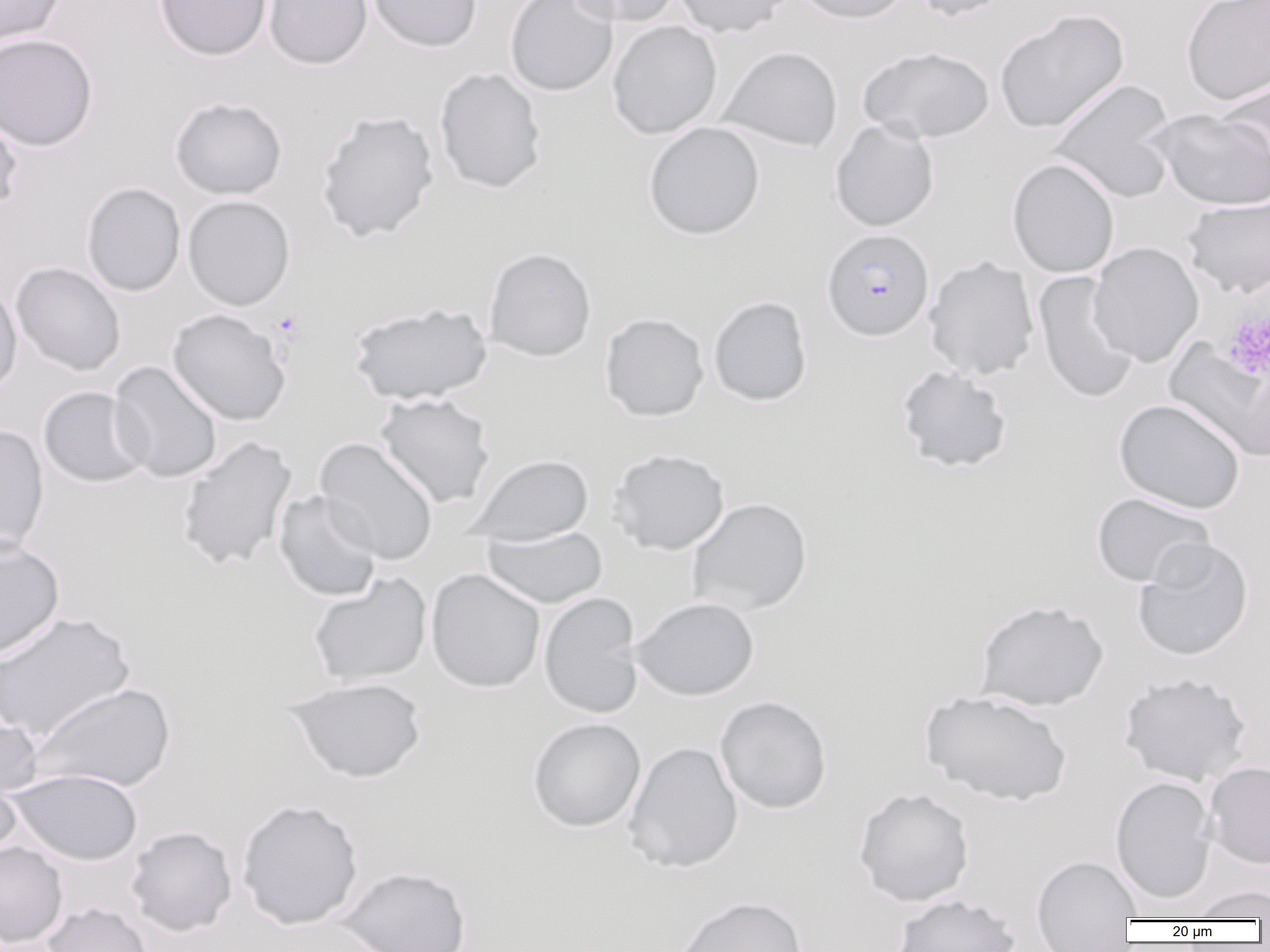
Summary:
  - Coordinate format: approximate bounding boxes as named x1/y1/x2/y2 corners in pixels
  - Platelet locations: (x1=1222, y1=309, x2=1270, y2=379)
  - Plasmodium falciparum-infected red blood cell locations: (x1=822, y1=228, x2=934, y2=341)
  - Uninfected red blood cell locations: (x1=0, y1=0, x2=67, y2=48), (x1=153, y1=0, x2=273, y2=61), (x1=263, y1=0, x2=372, y2=70), (x1=367, y1=0, x2=482, y2=53), (x1=504, y1=0, x2=620, y2=97), (x1=567, y1=0, x2=682, y2=27), (x1=673, y1=0, x2=793, y2=37), (x1=795, y1=0, x2=914, y2=24), (x1=909, y1=0, x2=1017, y2=22), (x1=1181, y1=0, x2=1270, y2=105), (x1=994, y1=8, x2=1130, y2=134), (x1=607, y1=21, x2=723, y2=139), (x1=0, y1=33, x2=99, y2=151), (x1=858, y1=45, x2=995, y2=144), (x1=719, y1=46, x2=843, y2=153), (x1=434, y1=67, x2=547, y2=194), (x1=1215, y1=77, x2=1270, y2=185), (x1=1049, y1=79, x2=1179, y2=203), (x1=169, y1=96, x2=288, y2=200), (x1=0, y1=107, x2=24, y2=217), (x1=1147, y1=108, x2=1270, y2=210), (x1=315, y1=110, x2=440, y2=242), (x1=829, y1=119, x2=940, y2=232), (x1=643, y1=122, x2=765, y2=240), (x1=1007, y1=158, x2=1120, y2=278), (x1=81, y1=182, x2=186, y2=297), (x1=182, y1=195, x2=295, y2=311), (x1=1182, y1=195, x2=1269, y2=299), (x1=1088, y1=242, x2=1204, y2=367), (x1=484, y1=247, x2=597, y2=361), (x1=923, y1=256, x2=1040, y2=382), (x1=10, y1=262, x2=126, y2=376), (x1=1033, y1=271, x2=1140, y2=404), (x1=0, y1=281, x2=22, y2=398), (x1=708, y1=295, x2=813, y2=407), (x1=348, y1=302, x2=492, y2=405), (x1=166, y1=309, x2=291, y2=426), (x1=600, y1=313, x2=709, y2=422), (x1=1166, y1=340, x2=1270, y2=461), (x1=109, y1=361, x2=223, y2=483), (x1=894, y1=364, x2=1014, y2=474), (x1=38, y1=386, x2=150, y2=488), (x1=375, y1=392, x2=496, y2=508), (x1=1113, y1=399, x2=1247, y2=514), (x1=0, y1=425, x2=49, y2=557), (x1=175, y1=436, x2=297, y2=572), (x1=315, y1=437, x2=439, y2=566), (x1=607, y1=448, x2=730, y2=555), (x1=467, y1=454, x2=594, y2=545), (x1=273, y1=490, x2=382, y2=602), (x1=1091, y1=492, x2=1215, y2=589), (x1=687, y1=497, x2=813, y2=616), (x1=481, y1=525, x2=608, y2=609), (x1=0, y1=536, x2=65, y2=661), (x1=1132, y1=538, x2=1255, y2=662), (x1=426, y1=569, x2=546, y2=693), (x1=307, y1=573, x2=432, y2=688), (x1=538, y1=591, x2=645, y2=719), (x1=632, y1=596, x2=759, y2=701), (x1=974, y1=599, x2=1109, y2=711), (x1=0, y1=611, x2=136, y2=744), (x1=1118, y1=671, x2=1254, y2=786), (x1=285, y1=677, x2=427, y2=783), (x1=29, y1=682, x2=176, y2=794), (x1=920, y1=690, x2=1073, y2=806), (x1=714, y1=696, x2=833, y2=814), (x1=0, y1=709, x2=44, y2=801), (x1=526, y1=717, x2=646, y2=833), (x1=622, y1=741, x2=743, y2=873), (x1=0, y1=760, x2=23, y2=863), (x1=1204, y1=761, x2=1270, y2=870), (x1=6, y1=768, x2=143, y2=866), (x1=1109, y1=776, x2=1218, y2=905), (x1=853, y1=786, x2=975, y2=907), (x1=237, y1=799, x2=363, y2=930), (x1=125, y1=825, x2=237, y2=936), (x1=0, y1=841, x2=68, y2=949), (x1=1031, y1=854, x2=1143, y2=950), (x1=335, y1=865, x2=472, y2=952), (x1=1187, y1=885, x2=1269, y2=920), (x1=891, y1=893, x2=1021, y2=952), (x1=671, y1=895, x2=808, y2=952), (x1=41, y1=902, x2=154, y2=952)
  - Slide-level diagnosis: Plasmodium falciparum
  - Image size: 1270×952 pixels
  - Field of view: single
  - Magnification: 1000x
  - Modality: light microscopy
  - Preparation: thin blood smear